Classify this cell by malaria status.
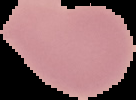
Uninfected.

The area outside the segmented cell region is set to black. From a thin blood film. Image is 136×100 pixels.